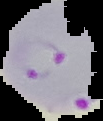
Cell region segmented out of the field of view; the surrounding area is masked to black. From a thin blood smear. Malaria status: parasitized. Image is 103×121 pixels.